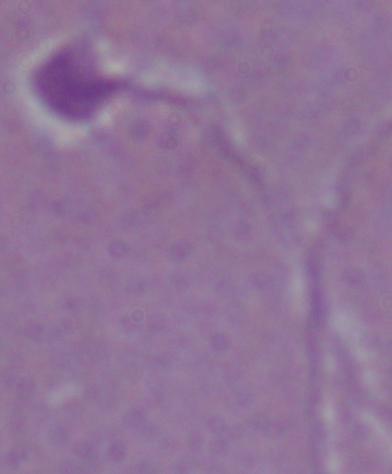
Summary:
  - Identification: Leishmania
  - Magnification: 1000x
  - Modality: photomicrograph